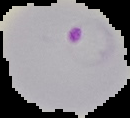
Summary:
  - Image size: 130×118 pixels
  - Preparation: thin blood film
  - Result: Plasmodium parasites identified
  - Image type: cell region segmented out of the field of view; surrounding area masked to black